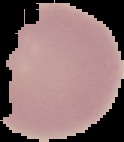

image type = segmented cell region on a black background
result = negative for Plasmodium parasites
preparation = thin blood film
image size = 124×142 pixels